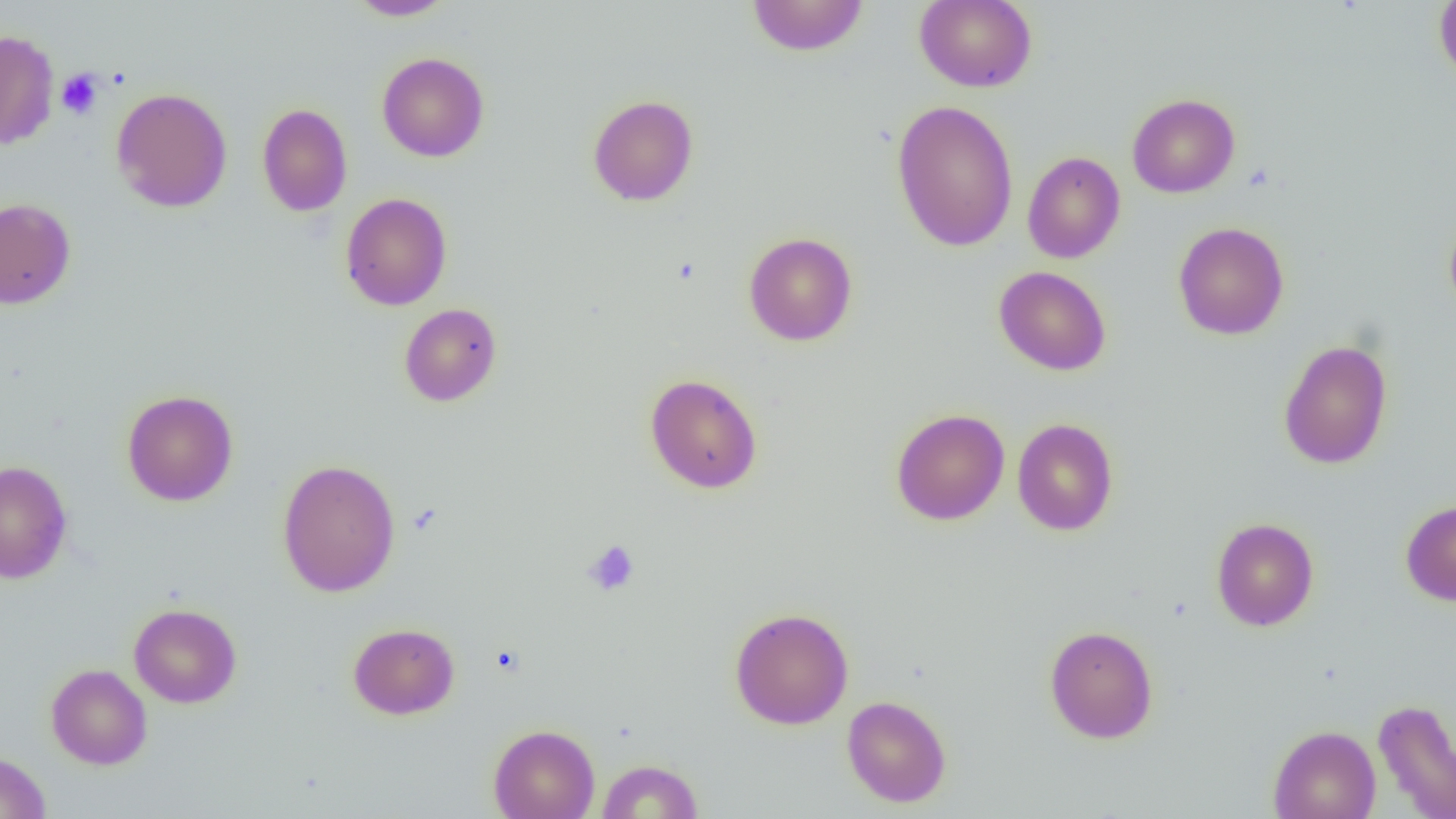

slide-level diagnosis = no evidence of blood parasites
field of view = single
platelet locations = approximate bounding boxes as (x1, y1, x2, y2) in pixels: (56, 68, 104, 119), (583, 540, 640, 596)
magnification = 1000x
modality = optical microscopy
uninfected red blood cell locations = approximate bounding boxes as (x1, y1, x2, y2) in pixels: (347, 0, 457, 21), (746, 0, 869, 57), (915, 0, 1037, 92), (1434, 0, 1456, 83), (0, 29, 59, 150), (376, 52, 489, 162), (111, 87, 232, 213), (1127, 93, 1240, 198), (587, 94, 699, 207), (891, 99, 1019, 253), (257, 102, 352, 216), (1022, 152, 1125, 263), (340, 192, 452, 311), (0, 197, 76, 310), (1444, 215, 1456, 319), (1173, 222, 1289, 340), (743, 232, 858, 346), (994, 266, 1112, 376), (399, 303, 502, 407), (1278, 339, 1393, 470), (644, 373, 762, 494), (122, 389, 238, 506), (891, 408, 1009, 526), (1012, 417, 1119, 536), (277, 459, 401, 597), (0, 460, 72, 584), (1400, 499, 1456, 606), (1211, 517, 1319, 631), (129, 603, 242, 708), (729, 607, 854, 729), (348, 622, 460, 720), (1044, 624, 1159, 743), (46, 664, 152, 770), (841, 695, 952, 807), (1372, 698, 1456, 819), (488, 724, 600, 819), (1268, 725, 1380, 819), (0, 751, 51, 819), (596, 759, 703, 818)
preparation = thin blood film
image size = 1456×819 pixels